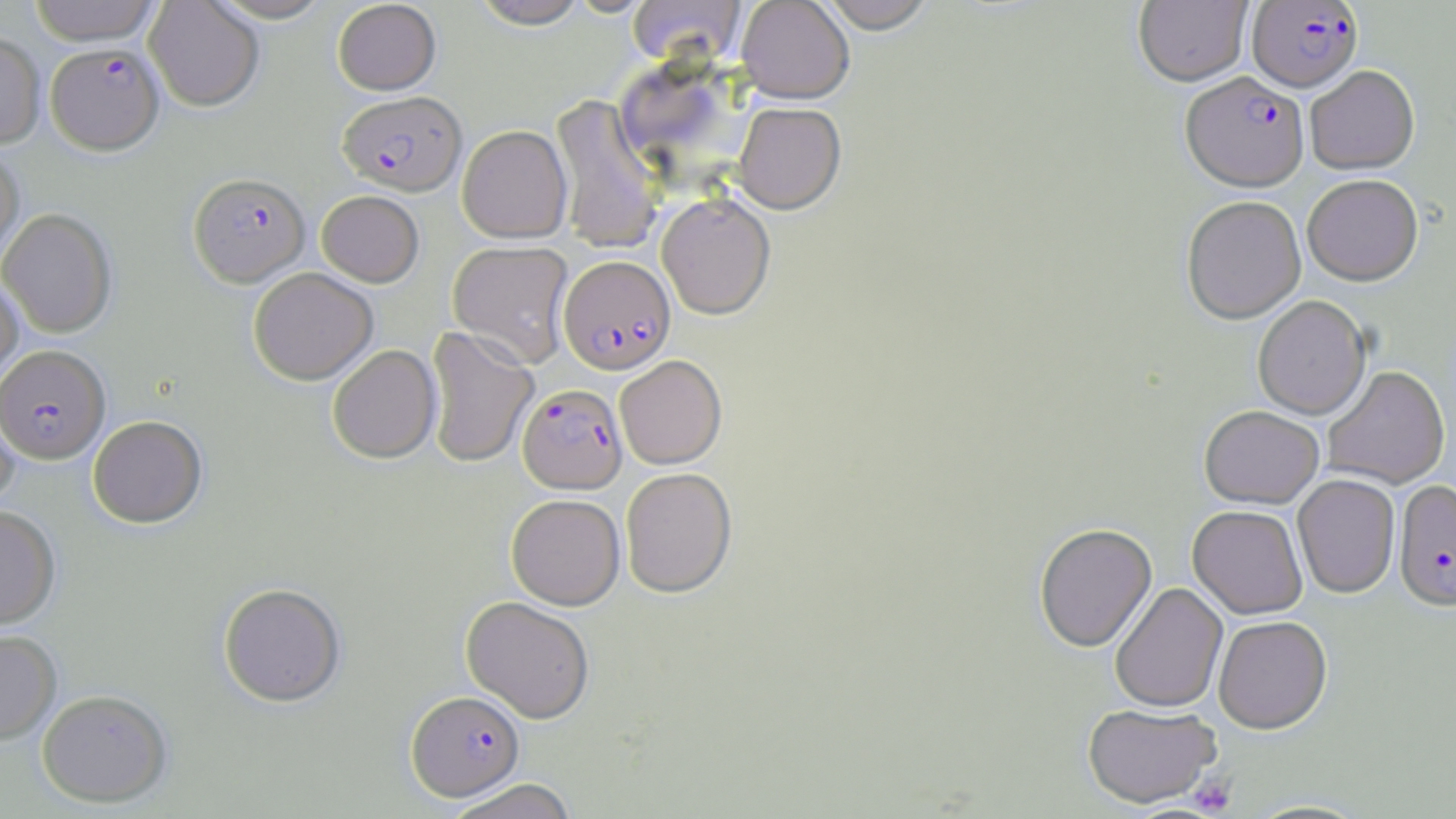

slide-level diagnosis = Plasmodium falciparum
uninfected red blood cell locations = approximate bounding boxes as (x1, y1, x2, y2) in pixels: (28, 0, 163, 45), (205, 0, 337, 23), (469, 0, 592, 30), (736, 0, 854, 104), (815, 0, 939, 37), (1134, 0, 1252, 87), (144, 1, 264, 111), (332, 1, 441, 95), (627, 1, 746, 68), (0, 31, 46, 148), (1305, 66, 1420, 175), (550, 93, 666, 254), (733, 103, 846, 215), (457, 125, 572, 243), (0, 146, 24, 266), (1302, 176, 1423, 287), (316, 190, 424, 287), (656, 193, 776, 320), (1181, 197, 1306, 324), (0, 208, 117, 338), (448, 240, 574, 367), (248, 267, 378, 385), (0, 273, 24, 388), (1253, 296, 1371, 420), (425, 326, 539, 469), (327, 344, 441, 464), (614, 356, 727, 469), (1322, 366, 1449, 489), (0, 393, 19, 513), (1199, 405, 1325, 509), (88, 415, 207, 528), (620, 467, 737, 597), (1292, 475, 1400, 598), (506, 494, 625, 610), (0, 505, 60, 629), (1188, 505, 1308, 619), (1034, 523, 1157, 653), (1110, 582, 1228, 713), (217, 583, 346, 707), (461, 596, 595, 723), (1213, 615, 1332, 733), (0, 629, 61, 744), (36, 688, 173, 807), (1082, 703, 1222, 808), (442, 778, 579, 819)
platelet locations = approximate bounding boxes as (x1, y1, x2, y2) in pixels: (1188, 773, 1237, 815)
magnification = 1000x
Plasmodium falciparum-infected red blood cell locations = approximate bounding boxes as (x1, y1, x2, y2) in pixels: (1248, 1, 1362, 92), (46, 42, 164, 154), (1181, 72, 1309, 193), (338, 91, 466, 196), (188, 172, 310, 287), (558, 255, 676, 375), (0, 345, 109, 463), (518, 383, 628, 493), (1393, 480, 1456, 611), (406, 690, 525, 801)
stain = May-Grünwald-Giemsa
modality = optical microscopy
image size = 1456×819 pixels
preparation = thin blood smear
field of view = single